Give the preparation type.
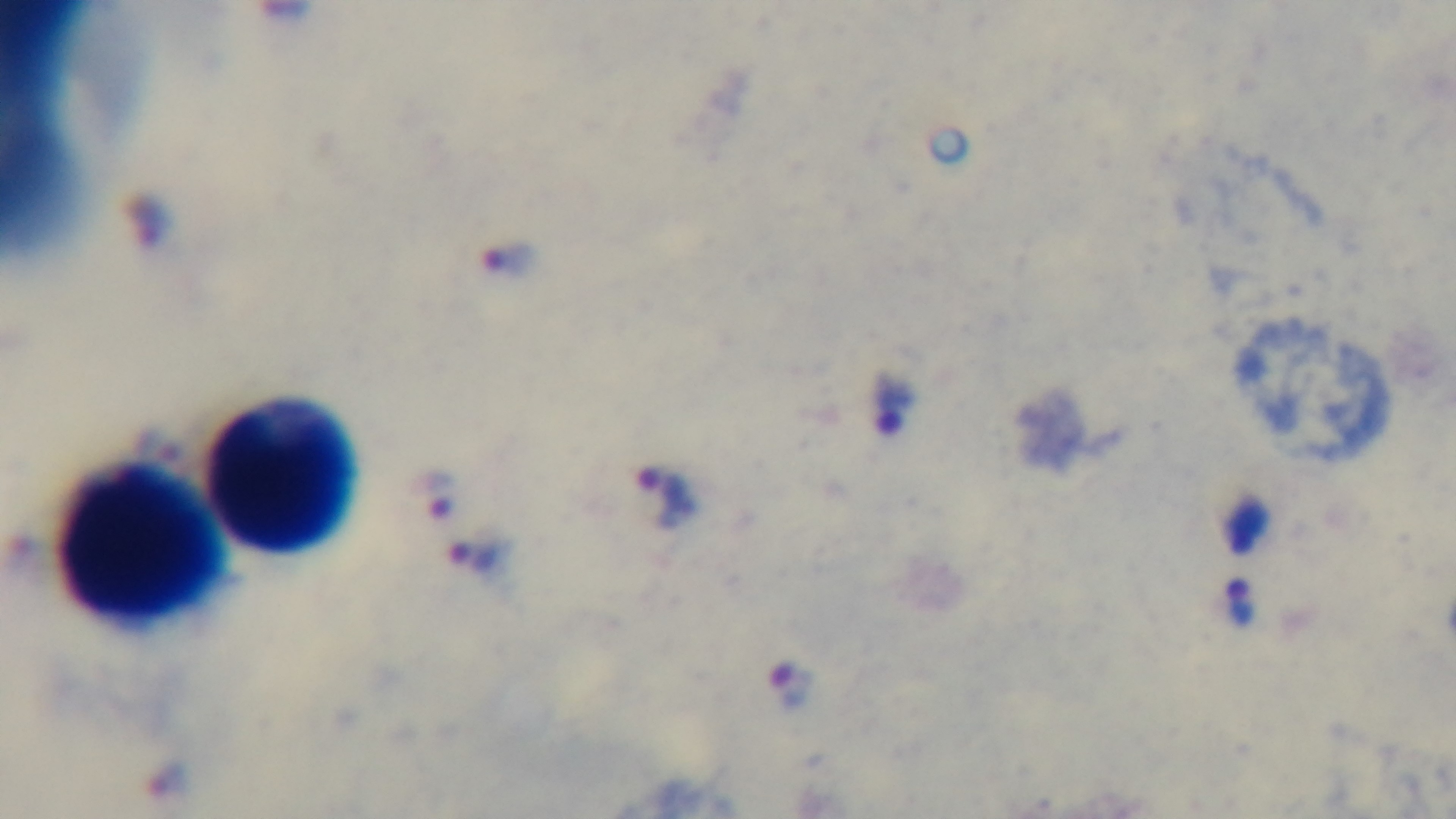
Thick.

Summary:
  - Objective: 100x oil immersion
  - Malaria status: infected
  - Stain: Giemsa
  - Modality: light microscopy
  - Capture: mounted 4K digital camera
  - Field of view: single